Locate every Trypanosoma brucei.
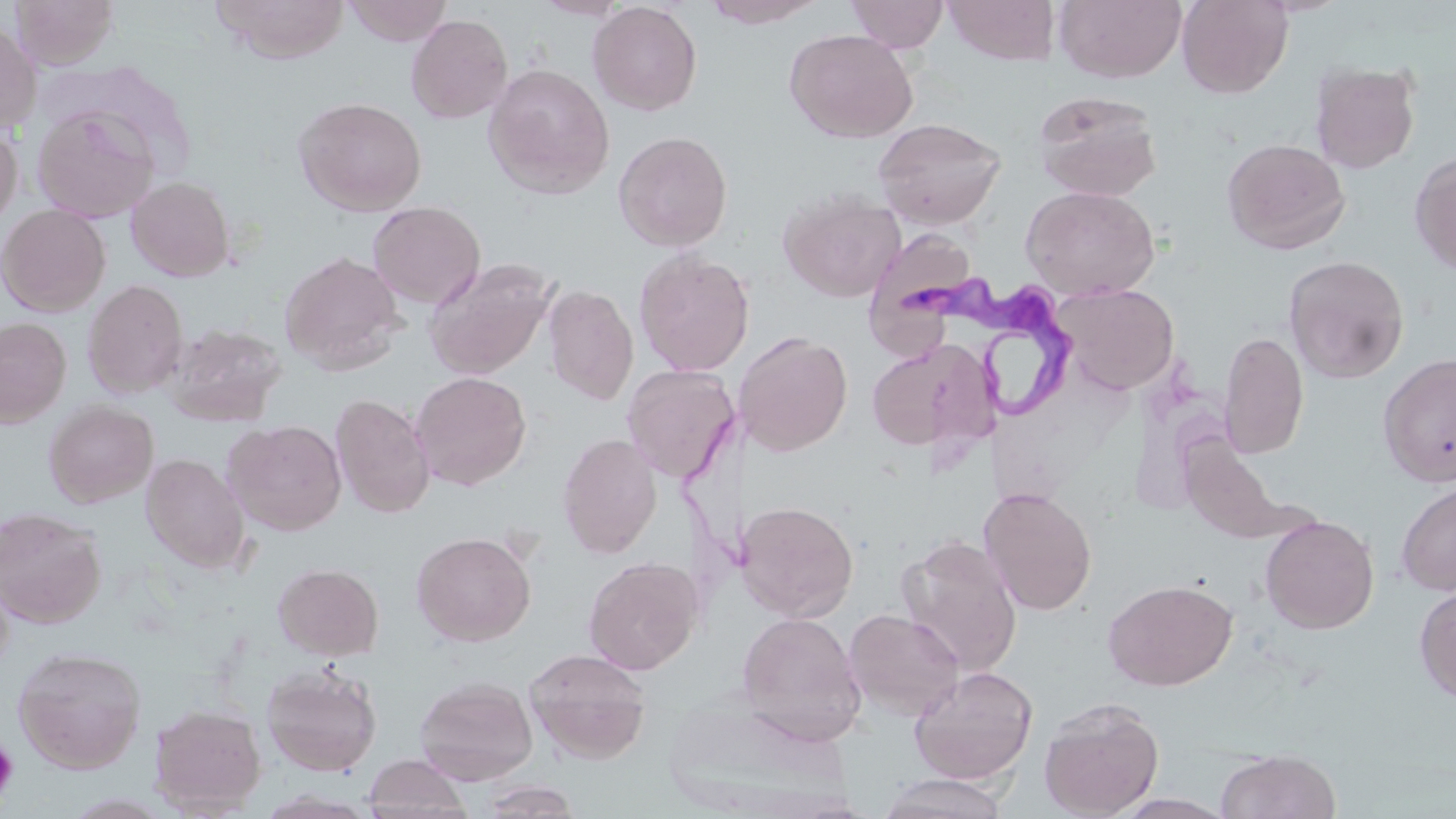

Approximate bounding boxes as (x1, y1, x2, y2) in pixels.
Trypanosoma brucei: (902, 277, 1090, 427).

slide_level_diagnosis: Trypanosoma brucei
preparation: thin blood film
image_size: 1456×819 pixels
uninfected_red_blood_cell_locations: 'approximate bounding boxes as (x1, y1, x2, y2) in pixels: (9, 0, 119, 69), (342, 0, 454, 46), (533, 0, 630, 20), (702, 0, 827, 28), (846, 0, 949, 53), (943, 0, 1060, 66), (1054, 0, 1187, 84), (1177, 0, 1293, 99), (213, 1, 350, 64), (588, 2, 703, 116), (406, 14, 513, 124), (0, 18, 42, 135), (783, 28, 919, 143), (1310, 61, 1421, 174), (482, 63, 615, 198), (1032, 90, 1164, 201), (293, 96, 428, 217), (30, 105, 160, 222), (873, 117, 1007, 230), (0, 121, 22, 233), (612, 130, 734, 252), (1221, 137, 1351, 254), (1409, 150, 1456, 274), (125, 176, 235, 282), (1021, 185, 1160, 299), (778, 189, 905, 302), (367, 201, 485, 309), (0, 204, 111, 317), (865, 229, 980, 357), (633, 248, 755, 376), (279, 250, 405, 375), (1284, 255, 1410, 383), (424, 257, 557, 380), (82, 279, 188, 398), (1054, 282, 1180, 395), (543, 284, 639, 405), (0, 317, 72, 428), (164, 322, 287, 427), (1219, 330, 1309, 459), (737, 331, 853, 456), (866, 339, 988, 454), (1378, 352, 1456, 488), (622, 364, 739, 484), (410, 371, 532, 490), (330, 393, 436, 519), (43, 400, 159, 508), (223, 419, 347, 536), (557, 433, 663, 558), (141, 453, 250, 574), (1395, 481, 1456, 596), (978, 487, 1098, 616), (736, 500, 859, 621), (0, 506, 107, 628), (1261, 515, 1379, 634), (411, 530, 537, 646), (896, 536, 1023, 676), (583, 556, 703, 675), (273, 563, 384, 661), (1102, 578, 1238, 691), (1414, 582, 1456, 705), (843, 609, 965, 722), (736, 611, 867, 746), (13, 645, 147, 774), (524, 648, 653, 764), (261, 661, 383, 777), (413, 664, 650, 775), (908, 665, 1039, 784), (414, 675, 538, 785), (661, 694, 851, 816), (1039, 696, 1164, 818), (148, 703, 266, 815), (1216, 748, 1341, 819), (362, 753, 472, 819), (875, 773, 1010, 819), (475, 779, 584, 818), (1111, 793, 1237, 818)'
platelet_locations: 'approximate bounding boxes as (x1, y1, x2, y2) in pixels: (0, 738, 18, 804)'
magnification: 1000x
stain: May-Grünwald-Giemsa
modality: optical microscopy
field_of_view: one of a larger specimen